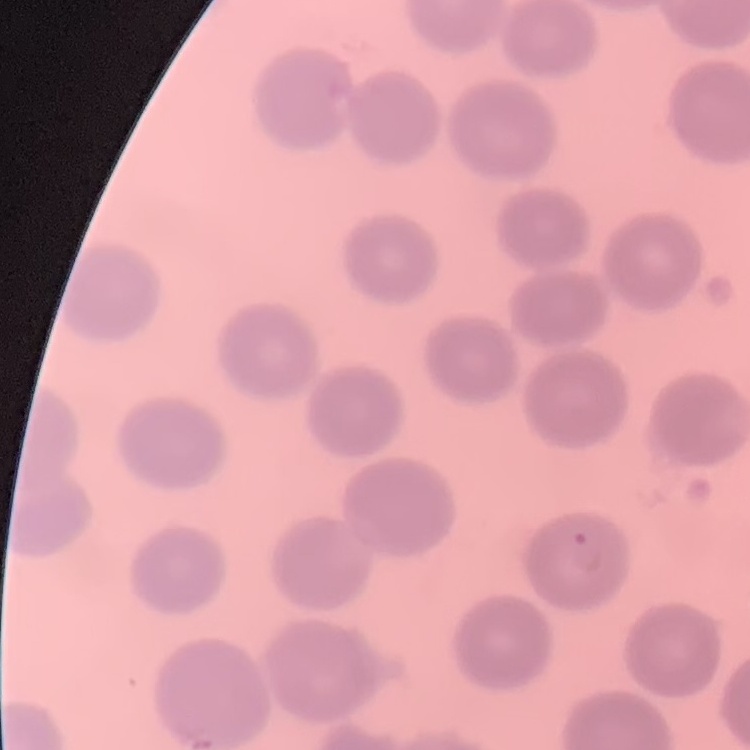
erythrocyte_morphology: no rouleaux formation
stain: Field's or Giemsa
preparation: thin blood film
image_type: one tile cut from a larger photomicrograph